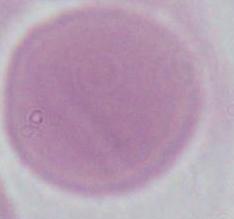

Summary:
  - Magnification: 1000x
  - Modality: micrograph
  - Identification: erythrocyte